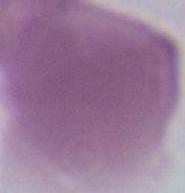
1000x magnification. A red blood cell is seen. Photomicrograph.